Give the position of every Plasmodium parasite visible.
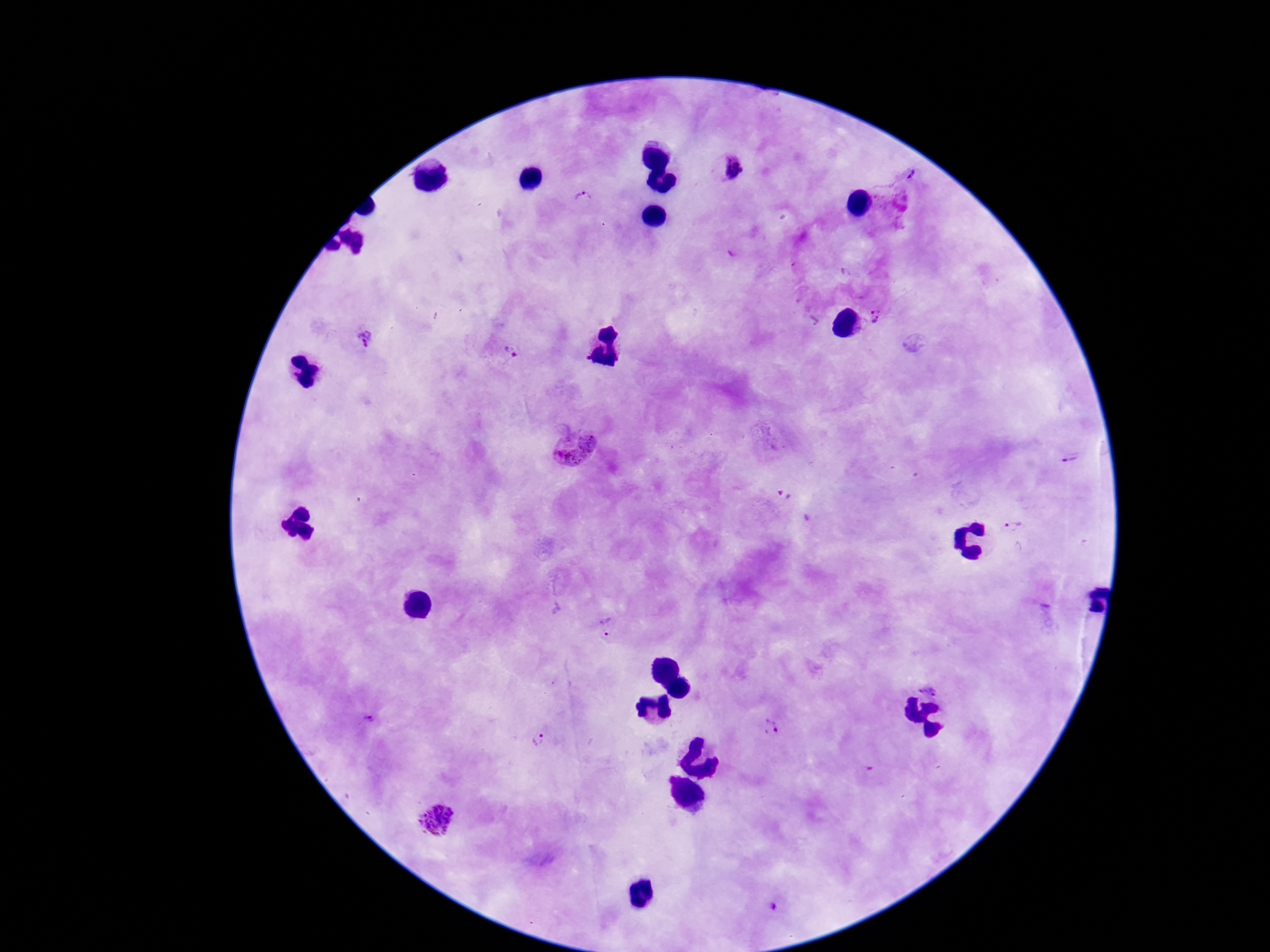

Approximate object centers, in pixels from the top-left corner.
Plasmodium parasites: (x=731, y=171), (x=910, y=174), (x=583, y=203), (x=876, y=318), (x=367, y=339), (x=512, y=352), (x=575, y=448), (x=1071, y=457), (x=1014, y=527), (x=607, y=626), (x=772, y=729), (x=541, y=738), (x=437, y=820), (x=773, y=906).

One field from this slide. Image is 1270×952 pixels. Patient malaria status: positive. Photographed through the microscope eyepiece with a smartphone camera. Giemsa stain. Thick blood film. 100x magnification.